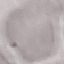 Malaria status: uninfected. Giemsa-stained preparation. Thin blood film. Acquired by smartphone through the microscope eyepiece. Cell patch, automatically extracted from a larger field of view and resized to 64 × 64 pixels.